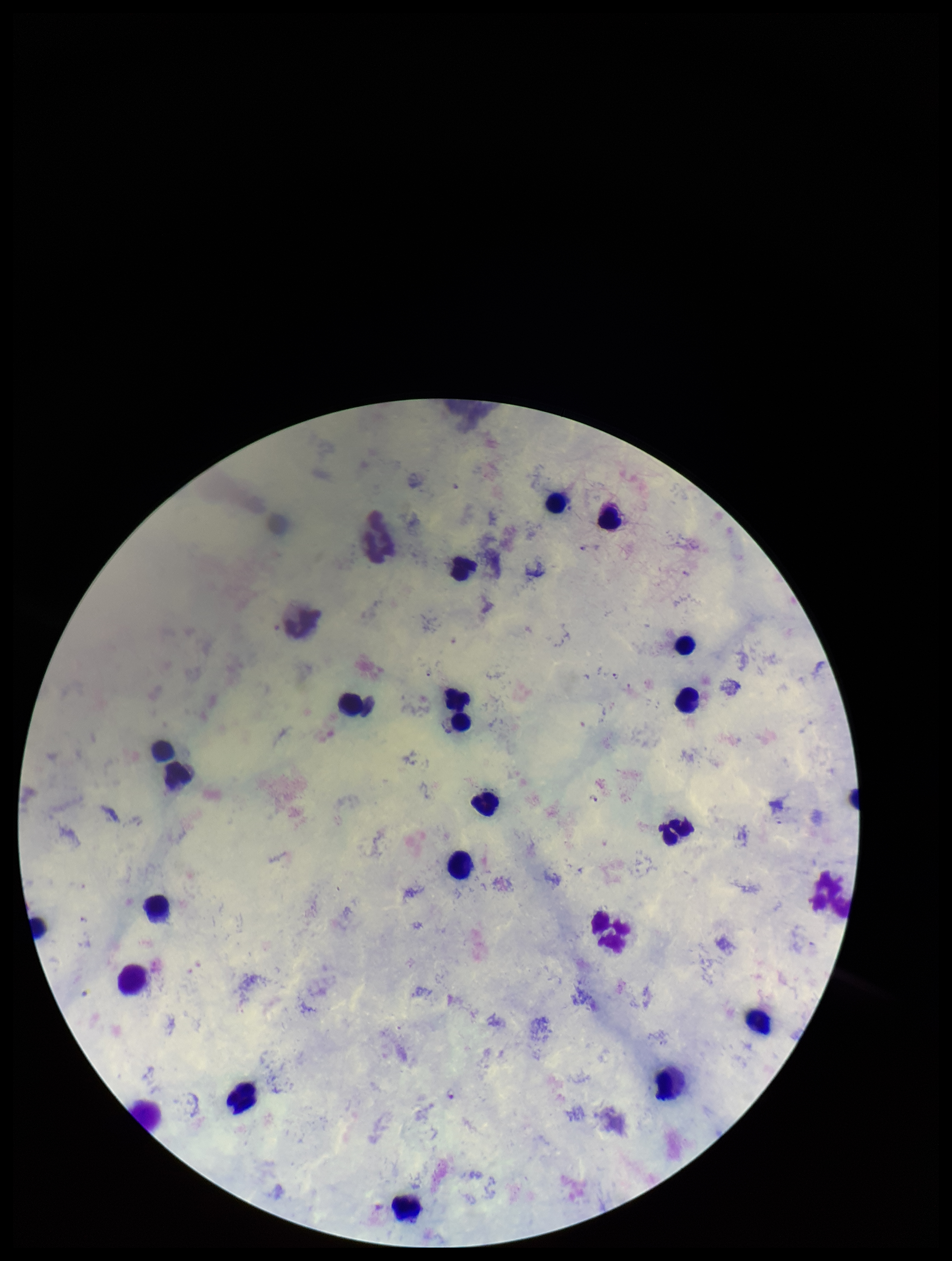 Patient malaria status: infected. Plasmodium parasites: identified. Leukocyte count: 22. Preparation: thick smear. Parasite count: 4. Image is 952×1261 pixels. Single field of view. Smartphone photograph taken through the eyepiece of a microscope. Species reported for this patient: Plasmodium falciparum. Giemsa stain.